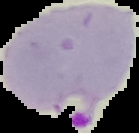 Malaria status: parasitized. Segmented cell region on a black background. Image is 139×133 pixels. From a thin blood smear.